Point out leukocytes.
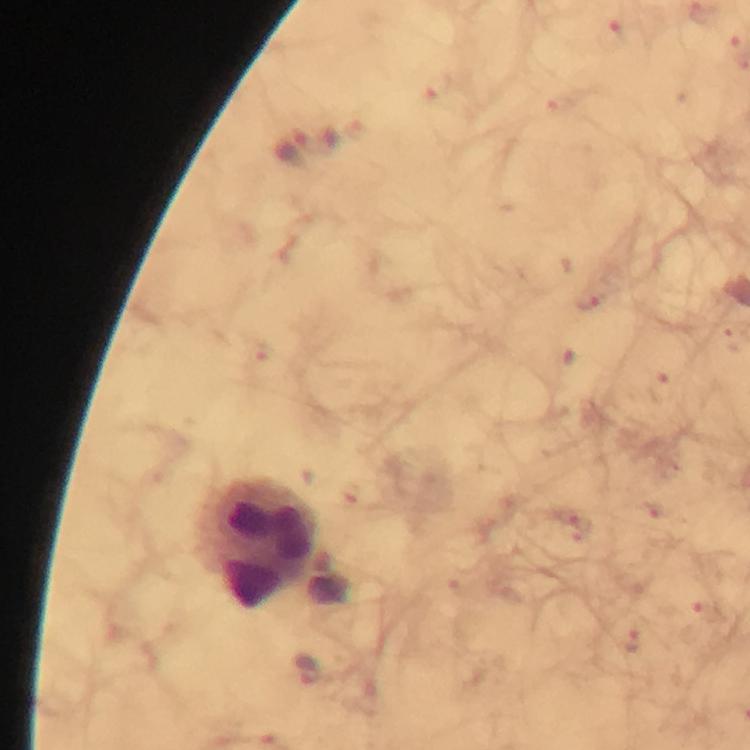
Approximate centers as {x, y} in pixels.
Leukocytes: {260, 543}.

{
  "magnification": "100x",
  "cropped_from": "one field of view",
  "capture": "smartphone photograph through a microscope",
  "image_size": "750×750 pixels",
  "context": "from a malaria diagnostic workup",
  "immersion_oil": "used",
  "preparation": "thick blood film",
  "stain": "Giemsa",
  "malaria_parasite_locations": "approximate centers as {x, y} in pixels: {609, 36}, {309, 667}"
}